Point out each leukocyte.
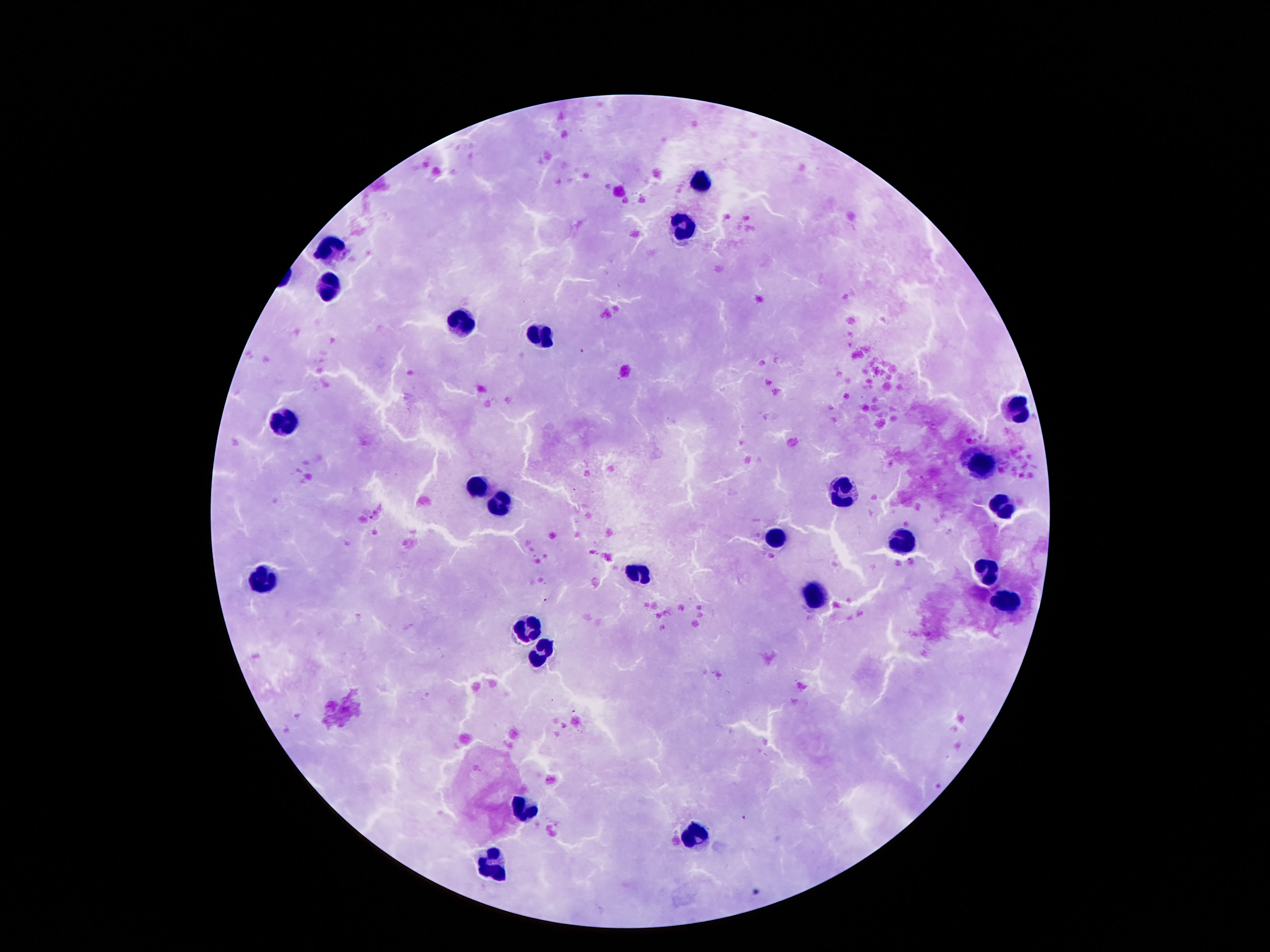
Approximate object centers, in pixels from the top-left corner.
Leukocytes: (x=702, y=184), (x=681, y=226), (x=328, y=248), (x=328, y=294), (x=460, y=322), (x=538, y=336), (x=1015, y=409), (x=284, y=422), (x=977, y=468), (x=477, y=487), (x=845, y=492), (x=503, y=506), (x=1000, y=506), (x=773, y=538), (x=902, y=544), (x=983, y=567), (x=637, y=574), (x=265, y=579), (x=813, y=594), (x=1004, y=602), (x=526, y=630), (x=542, y=649), (x=522, y=808), (x=698, y=835), (x=494, y=867).

Giemsa-stained preparation. Single field of view. Image is 1270×952 pixels. Patient malaria status: negative. Thick blood smear. 100x magnification. Smartphone photograph taken through the microscope eyepiece.